Assess this cell for malaria.
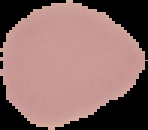
It is uninfected.

Summary:
  - Image size: 148×130 pixels
  - Image type: cell region segmented out of the field of view; surrounding area masked to black
  - Preparation: thin blood smear